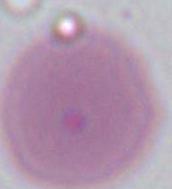
Summary:
  - Identification: erythrocyte
  - Magnification: 1000x
  - Modality: micrograph